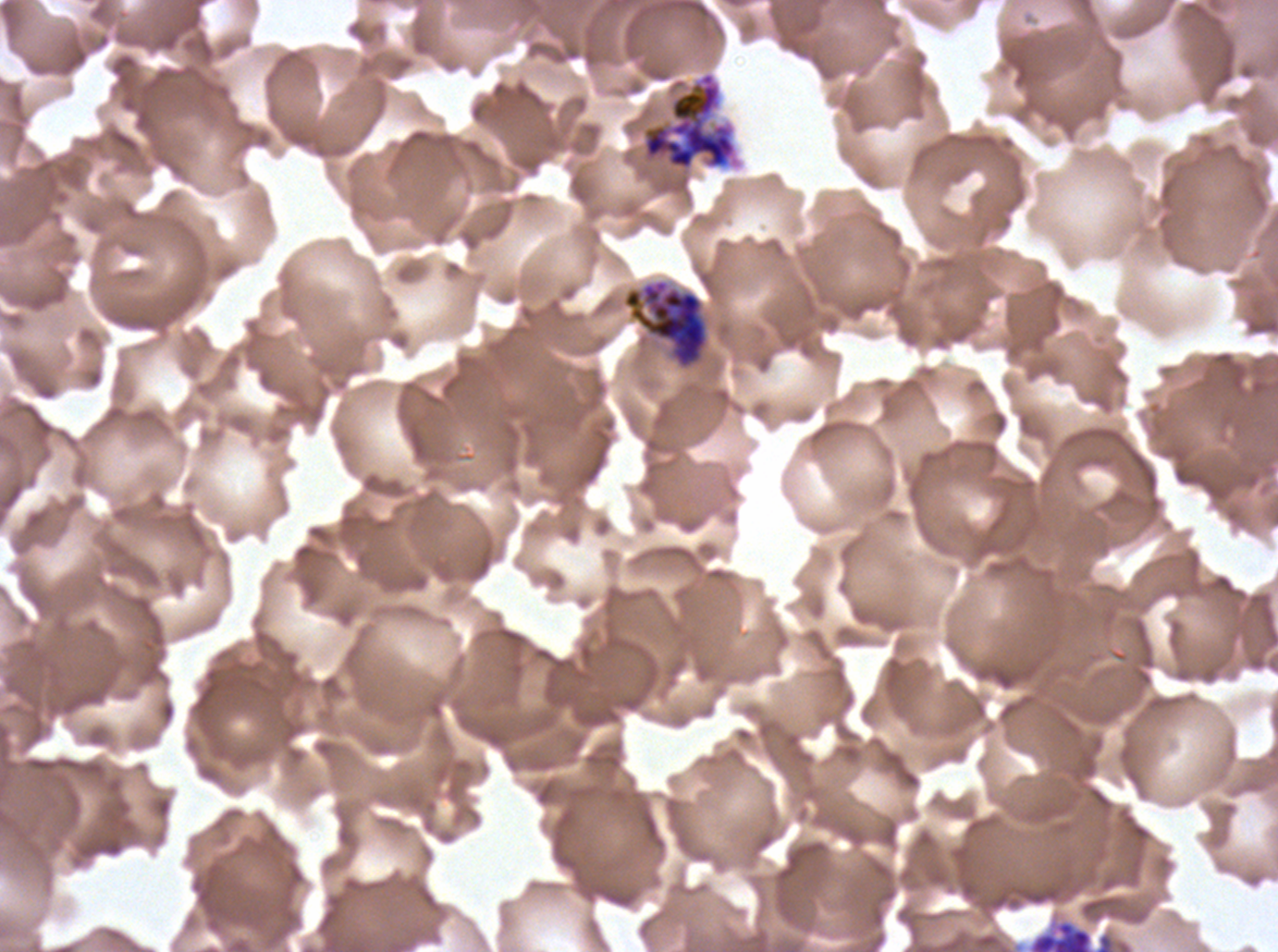
Approximate bounding rectangles given as corner coordinates in pixels from the top-left.
Summary:
  - Late schizont locations: (x1=641, y1=70, x2=741, y2=172), (x1=622, y1=279, x2=708, y2=368), (x1=1026, y1=917, x2=1095, y2=951)
  - Specimen: P. falciparum cultured ex vivo for 24 to 48 hours, from a patient in The Gambia
  - Field of view: sub-image separated from a larger composite
  - Preparation: thin blood smear
  - Image size: 1278×952 pixels
  - Stain: Giemsa